State which cell type is depicted.
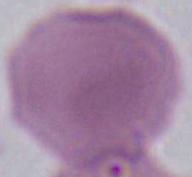

An erythrocyte.

Summary:
  - Modality: micrograph
  - Magnification: 1000x